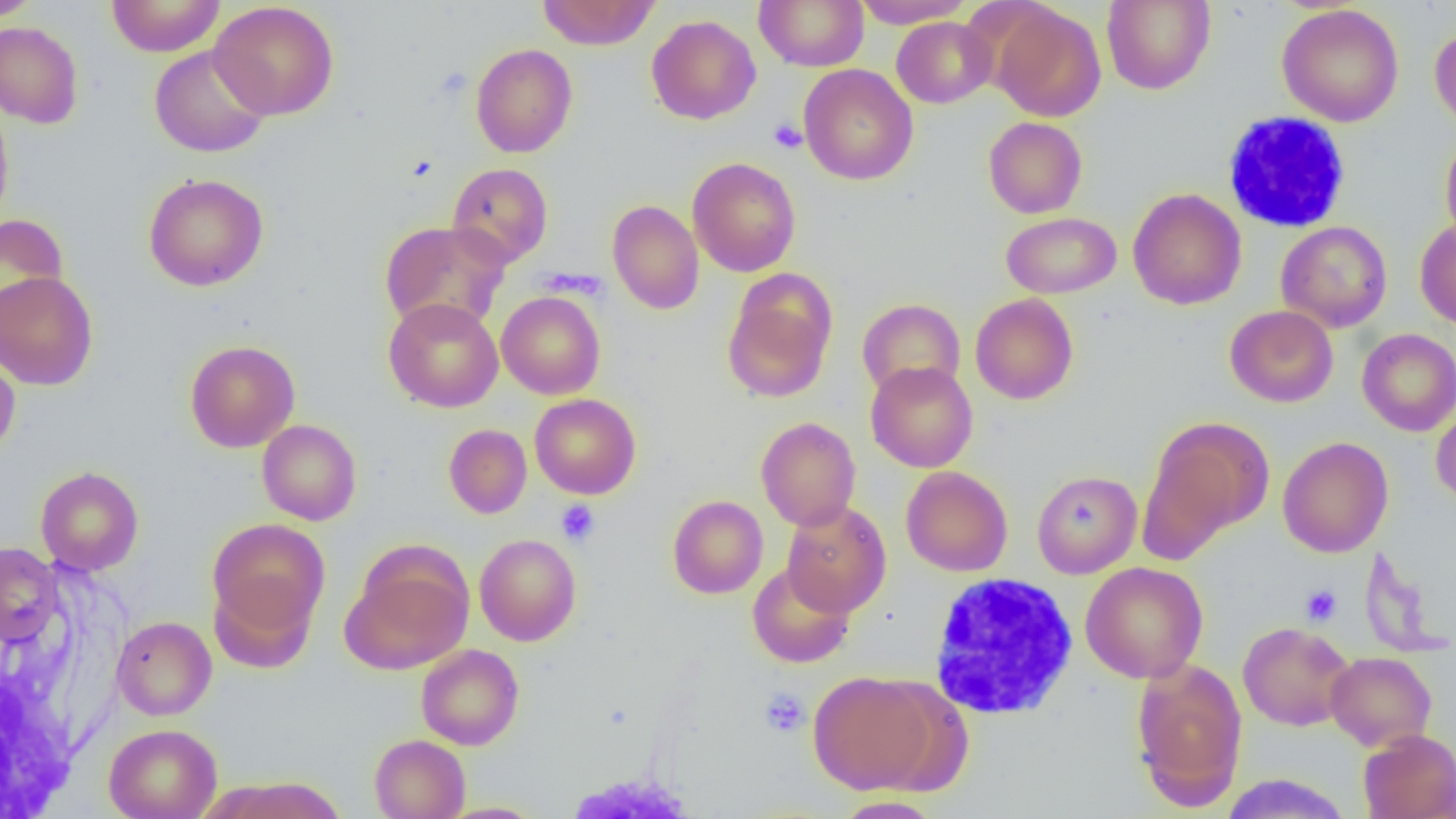
{
  "slide_level_diagnosis": "no evidence of blood parasites",
  "uninfected_red_blood_cell_locations": "approximate bounding boxes as (x1, y1, x2, y2) in pixels: (0, 0, 44, 22), (106, 0, 225, 57), (537, 0, 660, 50), (755, 0, 868, 71), (851, 0, 974, 28), (1102, 0, 1215, 94), (209, 1, 340, 121), (990, 3, 1106, 122), (1277, 4, 1404, 127), (646, 14, 761, 125), (892, 16, 996, 108), (0, 21, 84, 128), (1429, 24, 1456, 133), (471, 43, 577, 158), (149, 45, 271, 158), (799, 64, 918, 186), (0, 97, 14, 229), (983, 116, 1087, 218), (1440, 131, 1456, 247), (687, 157, 801, 277), (447, 162, 553, 267), (143, 173, 269, 291), (1128, 188, 1247, 310), (607, 199, 704, 314), (1000, 202, 1248, 302), (1000, 212, 1122, 299), (0, 214, 69, 331), (1415, 218, 1456, 331), (379, 219, 511, 333), (1276, 220, 1392, 333), (0, 271, 99, 390), (722, 278, 836, 402), (496, 291, 605, 399), (970, 294, 1078, 405), (383, 298, 503, 412), (857, 298, 965, 399), (1225, 305, 1338, 407), (1357, 328, 1456, 436), (185, 340, 300, 452), (0, 348, 20, 460), (866, 361, 978, 473), (530, 394, 641, 499), (1431, 401, 1456, 507), (756, 417, 861, 531), (1140, 417, 1274, 555), (257, 419, 362, 526), (443, 424, 532, 518), (1278, 436, 1393, 558), (35, 466, 144, 575), (901, 466, 1013, 577), (1032, 470, 1142, 578), (667, 495, 768, 599), (781, 501, 891, 616), (207, 518, 330, 637), (474, 534, 581, 646), (0, 542, 63, 647), (341, 554, 473, 675), (747, 561, 855, 668), (1080, 562, 1208, 683), (208, 577, 317, 673), (112, 616, 217, 720), (1238, 621, 1355, 731), (416, 644, 524, 750), (1326, 651, 1436, 751), (1130, 660, 1248, 808), (807, 670, 941, 794), (103, 724, 222, 819), (1358, 729, 1456, 819), (369, 734, 470, 818), (1219, 774, 1352, 818), (207, 776, 350, 818), (833, 795, 944, 818)",
  "platelet_locations": "approximate bounding boxes as (x1, y1, x2, y2) in pixels: (769, 119, 806, 153), (555, 499, 600, 546), (1300, 584, 1342, 626), (759, 688, 810, 737)",
  "white_blood_cell_locations": "approximate bounding boxes as (x1, y1, x2, y2) in pixels: (1221, 112, 1351, 233), (928, 574, 1078, 719)",
  "preparation": "thin blood film",
  "field_of_view": "single",
  "modality": "light microscopy",
  "magnification": "1000x",
  "image_size": "1456×819 pixels"
}